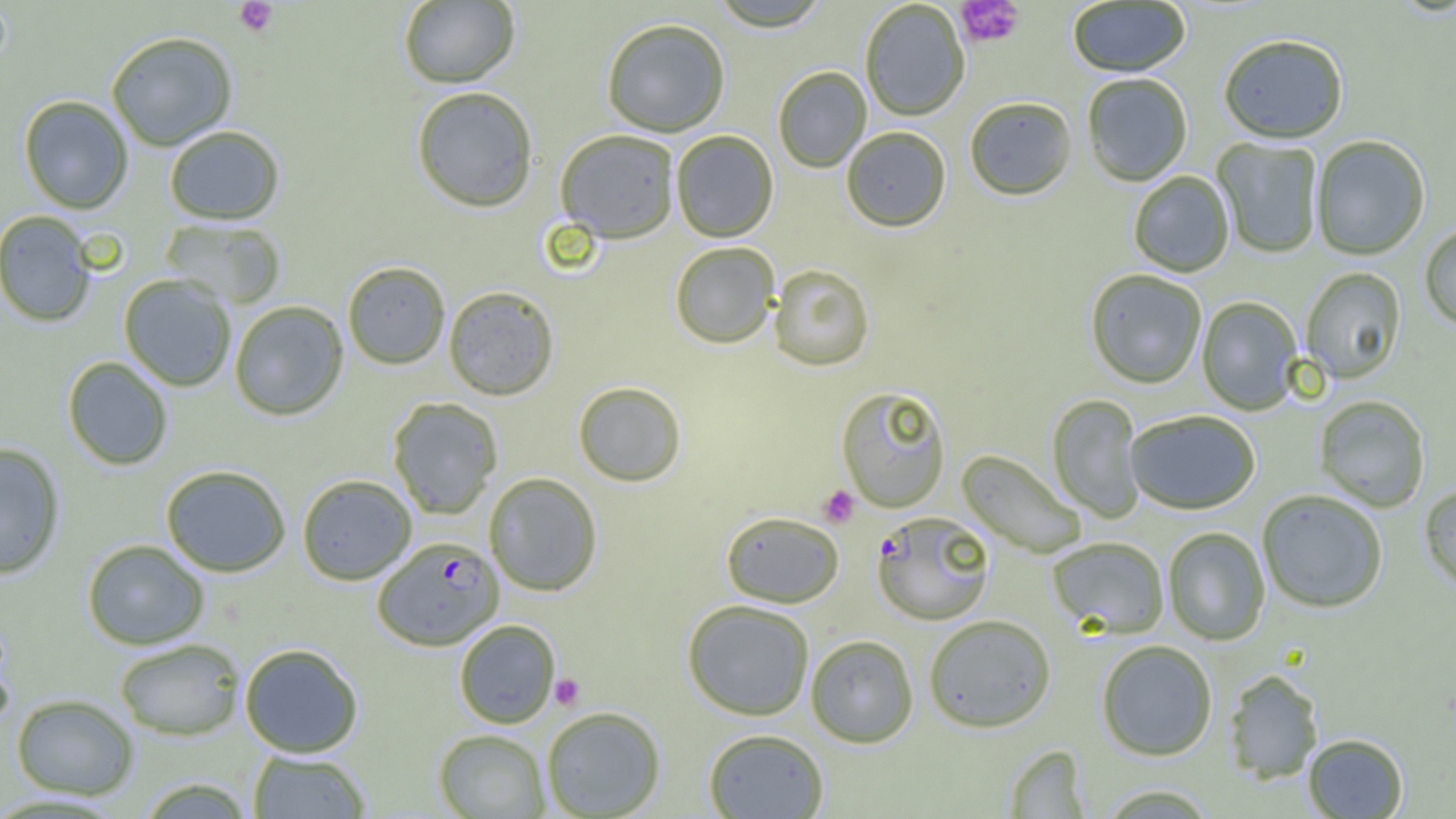
{
  "slide_level_diagnosis": "Plasmodium falciparum",
  "field_of_view": "single",
  "uninfected_red_blood_cell_locations": "approximate bounding boxes as (x1,y1)-(x2,y2) corner pairs in pixels: (708,0)-(833,33), (398,1)-(520,88), (1067,1)-(1191,78), (860,2)-(970,121), (601,18)-(731,137), (106,31)-(237,151), (1218,35)-(1349,145), (773,67)-(872,173), (1082,74)-(1193,186), (411,86)-(539,212), (18,95)-(134,214), (964,98)-(1077,202), (164,125)-(285,225), (841,127)-(951,233), (555,129)-(680,244), (671,130)-(778,242), (1312,136)-(1429,261), (1212,138)-(1323,258), (1128,172)-(1234,277), (1,211)-(97,327), (160,218)-(287,309), (1420,223)-(1456,332), (669,242)-(780,349), (342,261)-(451,369), (769,264)-(875,372), (1301,268)-(1406,384), (1085,270)-(1207,389), (119,274)-(237,391), (443,286)-(559,400), (1197,297)-(1303,415), (229,301)-(348,420), (62,356)-(173,470), (573,381)-(686,487), (835,386)-(951,513), (1047,394)-(1146,523), (1314,396)-(1430,512), (387,397)-(503,519), (1125,410)-(1260,515), (0,443)-(66,579), (957,450)-(1086,558), (160,464)-(291,577), (484,472)-(603,596), (297,474)-(417,585), (1419,486)-(1456,594), (1257,490)-(1387,614), (721,511)-(844,607), (1163,527)-(1270,645), (1047,537)-(1169,637), (81,539)-(209,650), (682,599)-(815,721), (923,614)-(1056,733), (454,619)-(561,728), (805,634)-(919,748), (114,638)-(244,740), (1096,640)-(1218,761), (239,643)-(364,757), (1223,670)-(1324,783), (11,693)-(139,800), (540,706)-(666,818), (703,728)-(829,818), (433,729)-(550,817), (1303,734)-(1408,818), (1004,744)-(1090,817), (247,750)-(371,818), (136,777)-(256,819), (1095,784)-(1220,818)",
  "modality": "light microscopy",
  "image_size": "1456×819 pixels",
  "magnification": "1000x",
  "platelet_locations": "approximate bounding boxes as (x1,y1)-(x2,y2) corner pairs in pixels: (233,0)-(279,37), (957,1)-(1024,48), (818,485)-(860,528), (550,673)-(586,710)",
  "preparation": "thin blood smear",
  "plasmodium_falciparum_infected_red_blood_cell_locations": "approximate bounding boxes as (x1,y1)-(x2,y2) corner pairs in pixels: (871,512)-(995,626), (372,537)-(504,650)"
}